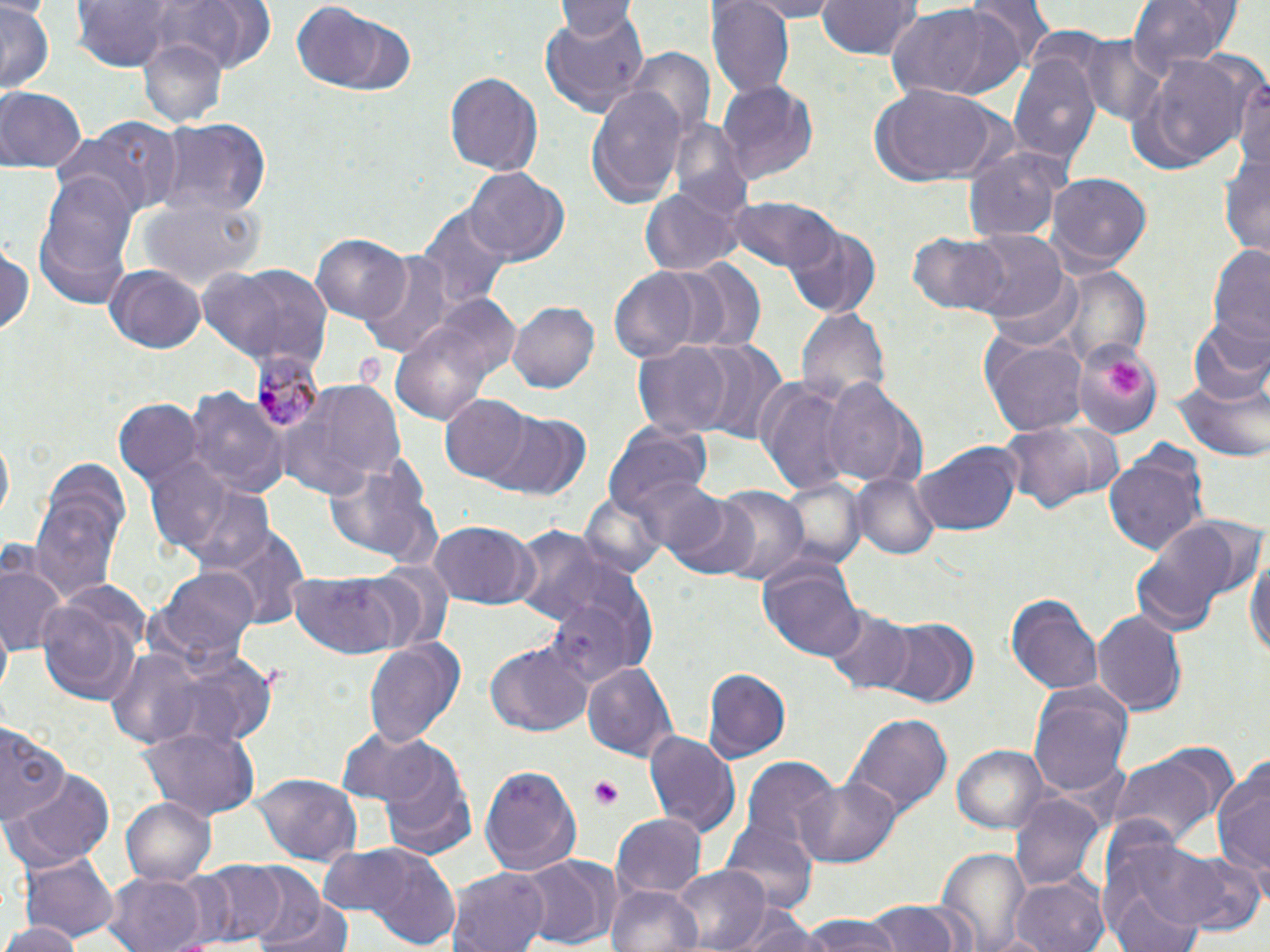 Approximate bounding boxes as [x1, y1, x2, y2] in pixels. Plasmodium malariae-infected red blood cell locations: [253, 349, 326, 431]. Platelet locations: [1109, 360, 1144, 397], [591, 778, 624, 809]. Uninfected red blood cell locations: [554, 0, 640, 38], [738, 0, 845, 20], [814, 0, 920, 60], [961, 0, 1054, 80], [1130, 0, 1235, 77], [709, 1, 794, 97], [69, 2, 186, 73], [0, 3, 54, 92], [291, 3, 418, 97], [884, 3, 1025, 103], [539, 8, 651, 119], [1072, 34, 1169, 127], [138, 36, 226, 129], [627, 48, 715, 141], [1123, 48, 1253, 177], [1008, 51, 1102, 167], [1231, 64, 1270, 177], [444, 70, 543, 178], [717, 80, 819, 187], [584, 82, 688, 206], [869, 83, 999, 185], [0, 87, 86, 174], [157, 118, 272, 223], [55, 119, 179, 214], [669, 119, 752, 215], [963, 143, 1069, 242], [1220, 147, 1270, 257], [463, 168, 565, 267], [36, 172, 140, 293], [1046, 173, 1153, 272], [640, 185, 742, 278], [723, 195, 843, 280], [135, 197, 266, 290], [419, 206, 512, 313], [782, 225, 881, 318], [961, 231, 1069, 322], [908, 232, 1010, 317], [311, 233, 411, 323], [1205, 243, 1270, 354], [0, 244, 34, 343], [359, 251, 458, 357], [670, 260, 766, 353], [198, 264, 330, 369], [104, 265, 206, 353], [609, 266, 703, 363], [1056, 266, 1151, 367], [506, 300, 599, 394], [798, 306, 889, 405], [387, 311, 512, 428], [1189, 321, 1270, 405], [980, 331, 1089, 435], [690, 336, 788, 444], [1074, 338, 1162, 438], [632, 340, 733, 438], [758, 377, 852, 500], [1173, 377, 1267, 460], [820, 378, 925, 492], [283, 381, 405, 496], [185, 386, 289, 498], [439, 395, 532, 484], [115, 399, 205, 498], [488, 413, 593, 500], [996, 420, 1120, 513], [605, 425, 711, 520], [915, 444, 1021, 535], [1104, 449, 1207, 560], [328, 456, 443, 568], [140, 457, 244, 552], [852, 472, 941, 561], [163, 474, 279, 574], [630, 474, 728, 561], [779, 476, 865, 567], [703, 485, 811, 586], [29, 490, 124, 603], [664, 491, 757, 577], [580, 492, 667, 578], [1128, 518, 1245, 634], [428, 519, 534, 609], [506, 522, 626, 624], [212, 527, 310, 630], [1244, 534, 1269, 665], [0, 547, 67, 658], [759, 561, 863, 660], [342, 565, 451, 654], [153, 567, 261, 667], [289, 570, 414, 662], [546, 581, 655, 686], [1008, 591, 1104, 698], [35, 592, 147, 705], [821, 607, 919, 695], [1092, 609, 1186, 718], [872, 616, 980, 709], [364, 638, 464, 748], [484, 641, 594, 737], [104, 647, 201, 746], [582, 662, 676, 762], [703, 667, 793, 762], [1026, 684, 1134, 802], [846, 714, 951, 818], [0, 720, 67, 829], [138, 724, 258, 823], [643, 729, 741, 837], [374, 744, 473, 853], [953, 745, 1047, 833], [1105, 745, 1230, 849], [739, 758, 839, 863], [1211, 759, 1270, 879], [478, 761, 583, 874], [6, 768, 116, 868], [254, 774, 361, 863], [794, 776, 900, 865], [1010, 793, 1102, 888], [120, 795, 215, 886], [612, 812, 706, 899], [720, 822, 816, 917], [1117, 838, 1266, 938], [322, 844, 463, 948], [937, 845, 1030, 952], [20, 852, 119, 946], [517, 857, 611, 949], [183, 861, 290, 946], [672, 864, 768, 952], [450, 865, 551, 952], [239, 866, 329, 946], [164, 868, 240, 949], [107, 872, 207, 952], [1009, 876, 1111, 952], [1105, 878, 1206, 952], [610, 884, 702, 952], [261, 895, 356, 952], [863, 900, 965, 952], [730, 910, 826, 952], [795, 917, 908, 952], [5, 918, 80, 952]. Slide-level diagnosis: Plasmodium malariae. Captured at 1000x magnification. Image is 1270×952 pixels. Light microscopy. One field of a larger specimen. May-Grünwald-Giemsa stain. Thin blood smear.